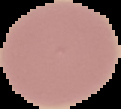

image type = segmented cell region with the area outside set to black
image size = 121×109 pixels
result = negative for Plasmodium parasites
preparation = thin blood smear